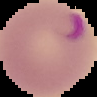

image type = segmented cell region with the area outside set to black
malaria status = parasitized
image size = 97×97 pixels
preparation = thin blood smear